Describe the morphology of the erythrocytes.
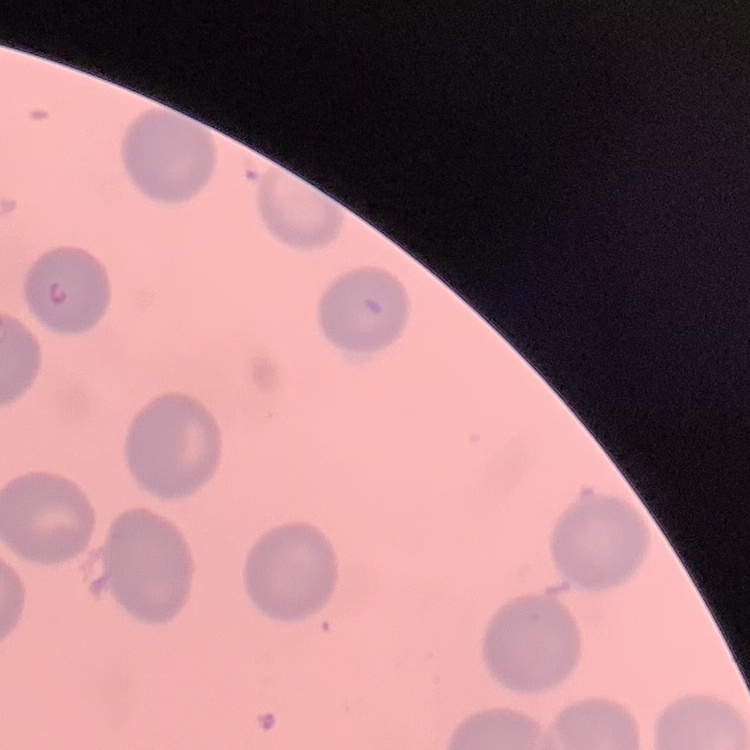
No rouleaux formation.

image_type: one tile cut from a larger photomicrograph
stain: Field's or Giemsa
preparation: thin blood film